Outline each blood parasite and name the species.
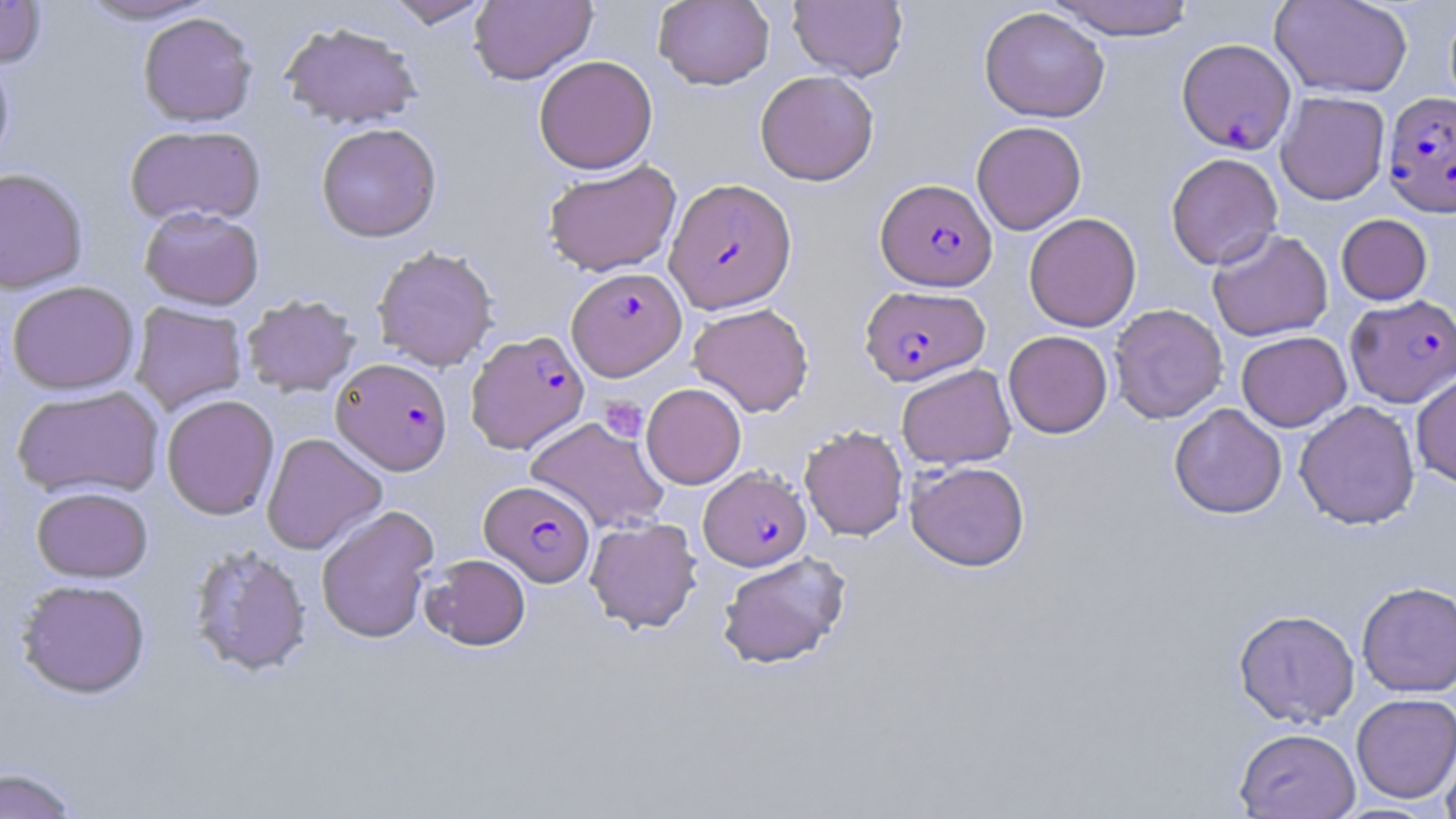

Approximate bounding boxes as named x1/y1/x2/y2 corners in pixels.
Plasmodium falciparum-infected red blood cells: (x1=1176, y1=38, x2=1296, y2=154), (x1=1383, y1=90, x2=1456, y2=217), (x1=665, y1=178, x2=797, y2=313), (x1=875, y1=178, x2=997, y2=291), (x1=567, y1=267, x2=687, y2=380), (x1=859, y1=285, x2=990, y2=386), (x1=1345, y1=294, x2=1456, y2=407), (x1=465, y1=330, x2=589, y2=454), (x1=331, y1=357, x2=452, y2=475), (x1=700, y1=466, x2=811, y2=571), (x1=480, y1=480, x2=594, y2=586).
No Plasmodium ovale, Plasmodium malariae, Plasmodium vivax, Babesia divergens, or Trypanosoma brucei observed.

Uninfected red blood cell locations: (x1=0, y1=0, x2=47, y2=68), (x1=73, y1=0, x2=220, y2=25), (x1=382, y1=0, x2=494, y2=28), (x1=469, y1=0, x2=597, y2=84), (x1=654, y1=0, x2=774, y2=90), (x1=788, y1=0, x2=907, y2=81), (x1=1044, y1=0, x2=1198, y2=40), (x1=1270, y1=0, x2=1413, y2=98), (x1=979, y1=6, x2=1110, y2=122), (x1=138, y1=12, x2=258, y2=126), (x1=280, y1=20, x2=423, y2=130), (x1=0, y1=51, x2=15, y2=171), (x1=533, y1=55, x2=658, y2=174), (x1=755, y1=70, x2=879, y2=185), (x1=1276, y1=91, x2=1390, y2=205), (x1=971, y1=120, x2=1086, y2=235), (x1=316, y1=122, x2=442, y2=242), (x1=125, y1=124, x2=266, y2=227), (x1=1165, y1=152, x2=1283, y2=271), (x1=542, y1=160, x2=682, y2=276), (x1=0, y1=167, x2=88, y2=293), (x1=139, y1=206, x2=265, y2=310), (x1=1024, y1=213, x2=1142, y2=332), (x1=1336, y1=214, x2=1432, y2=305), (x1=1207, y1=228, x2=1333, y2=341), (x1=372, y1=245, x2=499, y2=371), (x1=6, y1=280, x2=140, y2=395), (x1=241, y1=294, x2=360, y2=397), (x1=130, y1=302, x2=248, y2=415), (x1=688, y1=302, x2=814, y2=417), (x1=1108, y1=304, x2=1228, y2=423), (x1=1003, y1=330, x2=1112, y2=438), (x1=1236, y1=331, x2=1351, y2=432), (x1=896, y1=364, x2=1016, y2=469), (x1=1411, y1=371, x2=1456, y2=488), (x1=641, y1=383, x2=746, y2=489), (x1=12, y1=384, x2=164, y2=500), (x1=161, y1=394, x2=280, y2=520), (x1=1294, y1=400, x2=1420, y2=530), (x1=1169, y1=403, x2=1287, y2=519), (x1=525, y1=416, x2=670, y2=535), (x1=799, y1=424, x2=909, y2=541), (x1=261, y1=433, x2=387, y2=555), (x1=906, y1=460, x2=1030, y2=571), (x1=31, y1=486, x2=153, y2=582), (x1=316, y1=506, x2=438, y2=644), (x1=584, y1=517, x2=702, y2=633), (x1=188, y1=544, x2=312, y2=677), (x1=716, y1=551, x2=851, y2=670), (x1=421, y1=553, x2=531, y2=651), (x1=15, y1=578, x2=151, y2=698), (x1=1356, y1=580, x2=1456, y2=697), (x1=1233, y1=609, x2=1360, y2=727), (x1=1351, y1=693, x2=1456, y2=803), (x1=1439, y1=726, x2=1456, y2=819), (x1=1234, y1=727, x2=1360, y2=818), (x1=0, y1=766, x2=83, y2=818). Platelet locations: (x1=599, y1=396, x2=648, y2=442). Slide-level diagnosis: Plasmodium falciparum. Image is 1456×819 pixels. Optical microscopy. Thin blood smear. 1000x magnification. Single field of view. May-Grünwald-Giemsa stain.